State which parasite is depicted.
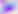
This is Toxoplasma gondii.

Summary:
  - Modality: photomicrograph
  - Magnification: 400x